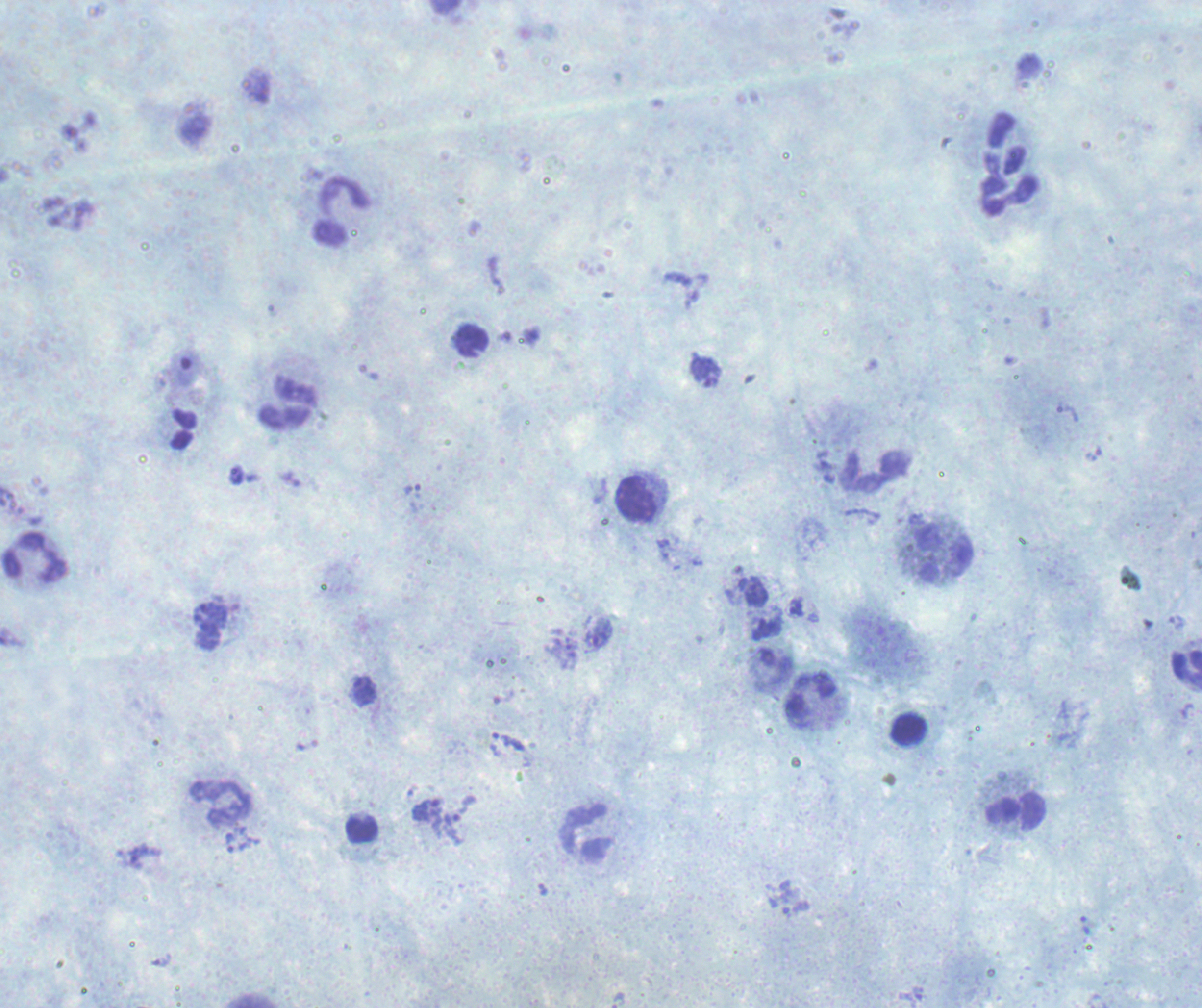

Romanowsky-stained preparation. Thick blood smear. One field from this slide. Image is 1202×1008 pixels.